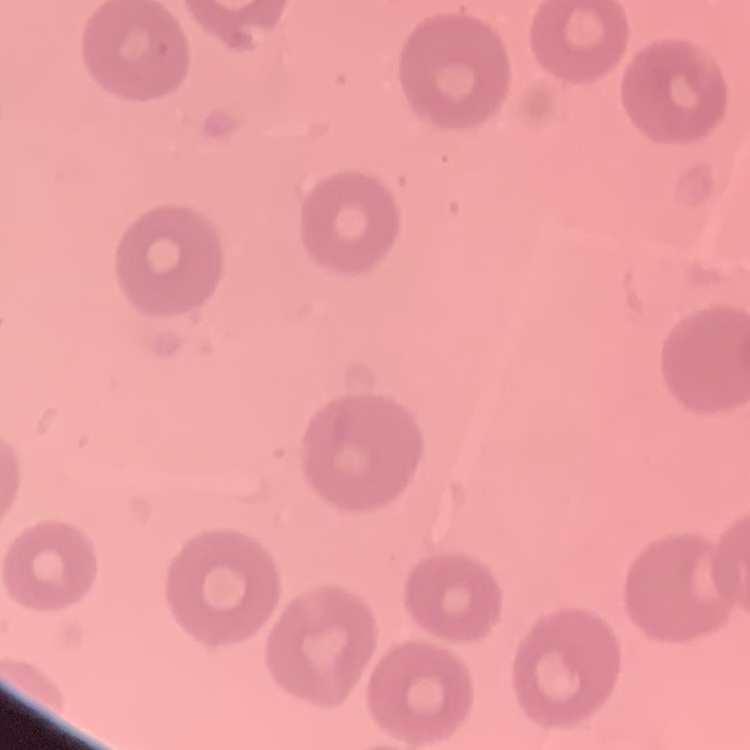 The red blood cells show no rouleaux formation. One tile cut from a larger photomicrograph. Stained with either Field's or Giemsa. Thin blood smear.